Locate every uninfected red blood cell.
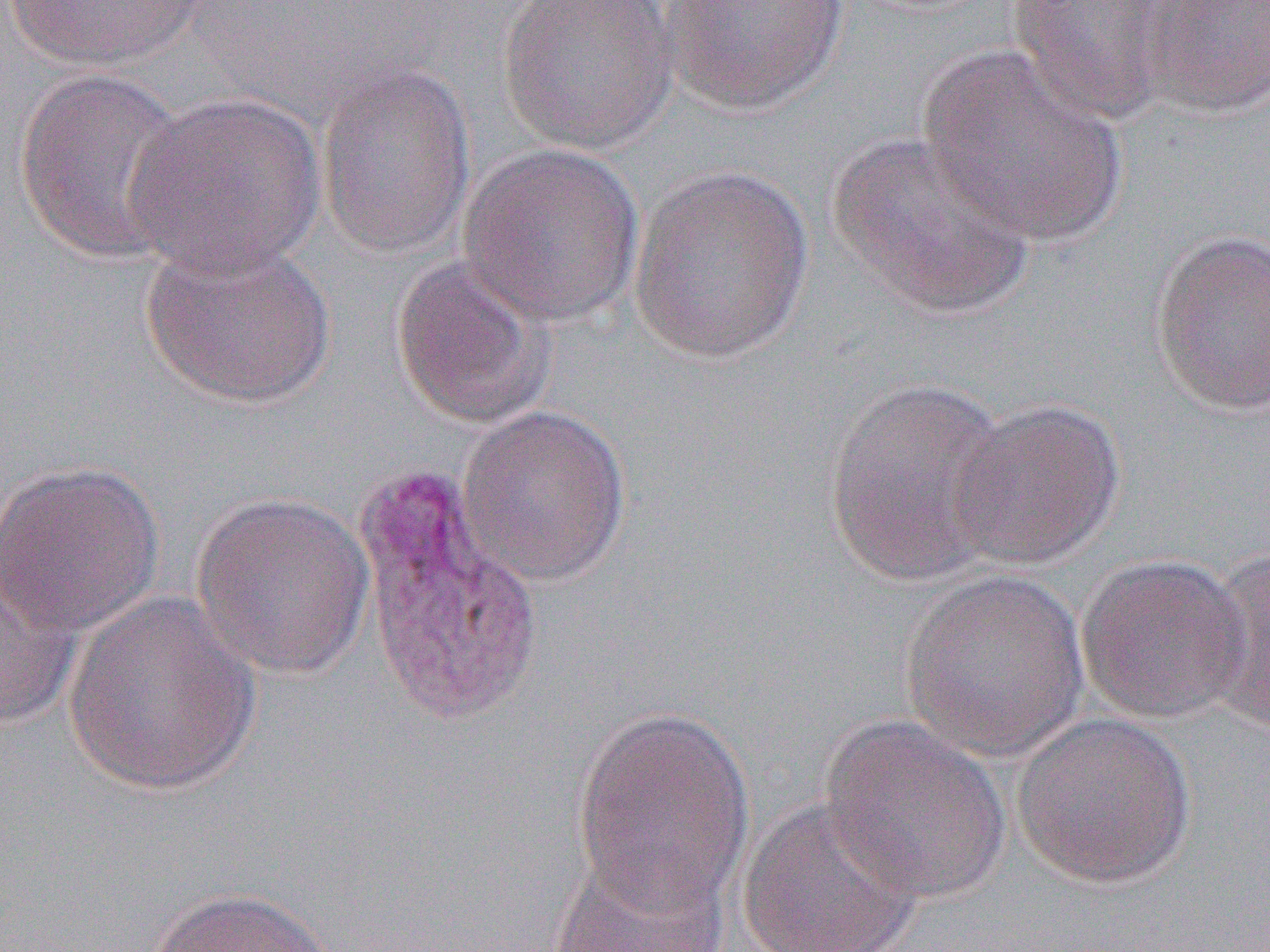
Approximate bounding boxes as named x1/y1/x2/y2 corners in pixels.
Uninfected red blood cells: (x1=3, y1=0, x2=211, y2=69), (x1=496, y1=0, x2=679, y2=155), (x1=654, y1=0, x2=853, y2=116), (x1=1136, y1=0, x2=1270, y2=119), (x1=1004, y1=1, x2=1181, y2=126), (x1=918, y1=44, x2=1128, y2=247), (x1=316, y1=60, x2=476, y2=260), (x1=12, y1=68, x2=193, y2=266), (x1=122, y1=91, x2=326, y2=279), (x1=822, y1=130, x2=1037, y2=319), (x1=458, y1=144, x2=644, y2=327), (x1=627, y1=163, x2=815, y2=365), (x1=1149, y1=229, x2=1270, y2=417), (x1=138, y1=236, x2=336, y2=408), (x1=389, y1=255, x2=557, y2=430), (x1=823, y1=375, x2=1014, y2=589), (x1=945, y1=398, x2=1126, y2=570), (x1=458, y1=403, x2=631, y2=586), (x1=0, y1=460, x2=166, y2=639), (x1=191, y1=491, x2=377, y2=680), (x1=1198, y1=549, x2=1270, y2=733), (x1=1077, y1=553, x2=1252, y2=724), (x1=0, y1=556, x2=83, y2=732), (x1=899, y1=568, x2=1091, y2=761), (x1=61, y1=593, x2=262, y2=798), (x1=569, y1=704, x2=757, y2=918), (x1=1010, y1=711, x2=1196, y2=889), (x1=818, y1=714, x2=1011, y2=904), (x1=735, y1=794, x2=925, y2=952), (x1=547, y1=855, x2=732, y2=952), (x1=148, y1=886, x2=342, y2=952).

Slide-level diagnosis: Plasmodium vivax. Optical microscopy. Captured at 1000x magnification. Thin blood smear. Single field of view. Image is 1270×952 pixels.